Report the malaria status of this cell.
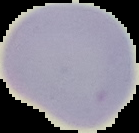

Uninfected.

image type = segmented cell region on a black background
image size = 139×133 pixels
preparation = thin blood smear